Point out every Plasmodium parasite and every leukocyte.
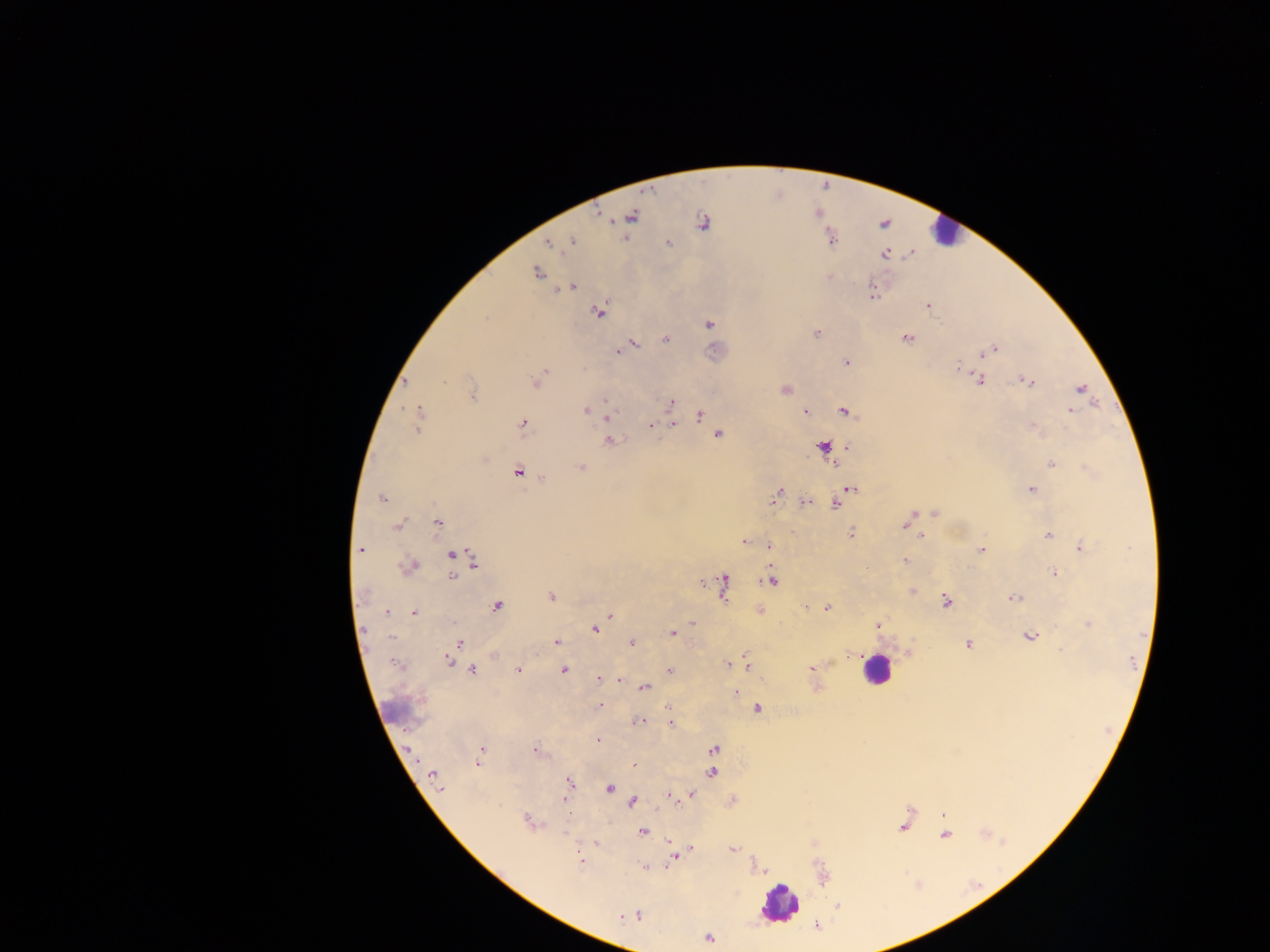

Approximate centers as (x, y) in pixels.
Plasmodium parasites: (631, 216), (702, 224), (573, 241), (667, 243), (549, 244), (885, 254), (536, 273), (829, 277), (571, 287), (873, 293), (928, 305), (599, 311), (486, 318), (709, 324), (817, 334), (665, 339), (906, 339), (634, 344), (993, 350), (618, 351), (984, 354), (847, 363), (959, 368), (544, 373), (980, 380), (444, 381), (1028, 381), (405, 382), (536, 382), (786, 389), (1081, 389), (473, 394), (606, 401), (671, 403), (585, 410), (420, 411), (1070, 411), (805, 412), (846, 412), (700, 414), (607, 418), (674, 423), (522, 424), (651, 425), (1033, 428), (417, 429), (718, 434), (609, 441), (823, 447), (1052, 462), (580, 467), (517, 471), (542, 479), (852, 489), (1031, 489), (780, 491), (776, 497), (382, 499), (806, 502), (835, 505), (934, 513), (907, 522), (437, 523), (398, 526), (850, 533), (1048, 534), (921, 536), (744, 541), (769, 546), (1081, 548), (360, 549), (981, 549), (451, 554), (474, 561), (904, 561), (409, 566), (1054, 573), (453, 575), (771, 580), (702, 582), (723, 583), (912, 591), (551, 596), (1014, 597), (946, 601), (497, 605), (806, 607), (826, 608), (388, 611), (413, 612), (610, 616), (693, 623), (1089, 624), (878, 626), (363, 629), (595, 629), (672, 633), (392, 636), (1030, 636), (556, 642), (632, 642), (459, 643), (968, 644), (1060, 650), (495, 656), (851, 656), (448, 661), (728, 665), (747, 665), (811, 667), (518, 669), (472, 670), (563, 670), (670, 670), (598, 679), (619, 680), (645, 688), (736, 691), (600, 706), (668, 708), (758, 708), (640, 721), (671, 723), (598, 740), (713, 749), (481, 750), (535, 751), (478, 762), (634, 765), (712, 772), (433, 776), (569, 782), (609, 788), (440, 789), (692, 794), (670, 795), (565, 799), (632, 802), (942, 815), (528, 821), (642, 831), (945, 835), (596, 843), (670, 844), (691, 847), (732, 849), (672, 857), (579, 859), (644, 867), (838, 906), (637, 915), (622, 916), (709, 938).
Leukocytes: (942, 231), (875, 670), (779, 903).

country = Ghana
field of view = single
image size = 1270×952 pixels
capture = mobile-phone photograph through a microscope
preparation = thick blood smear